Locate every Plasmodium ovale-infected red blood cell.
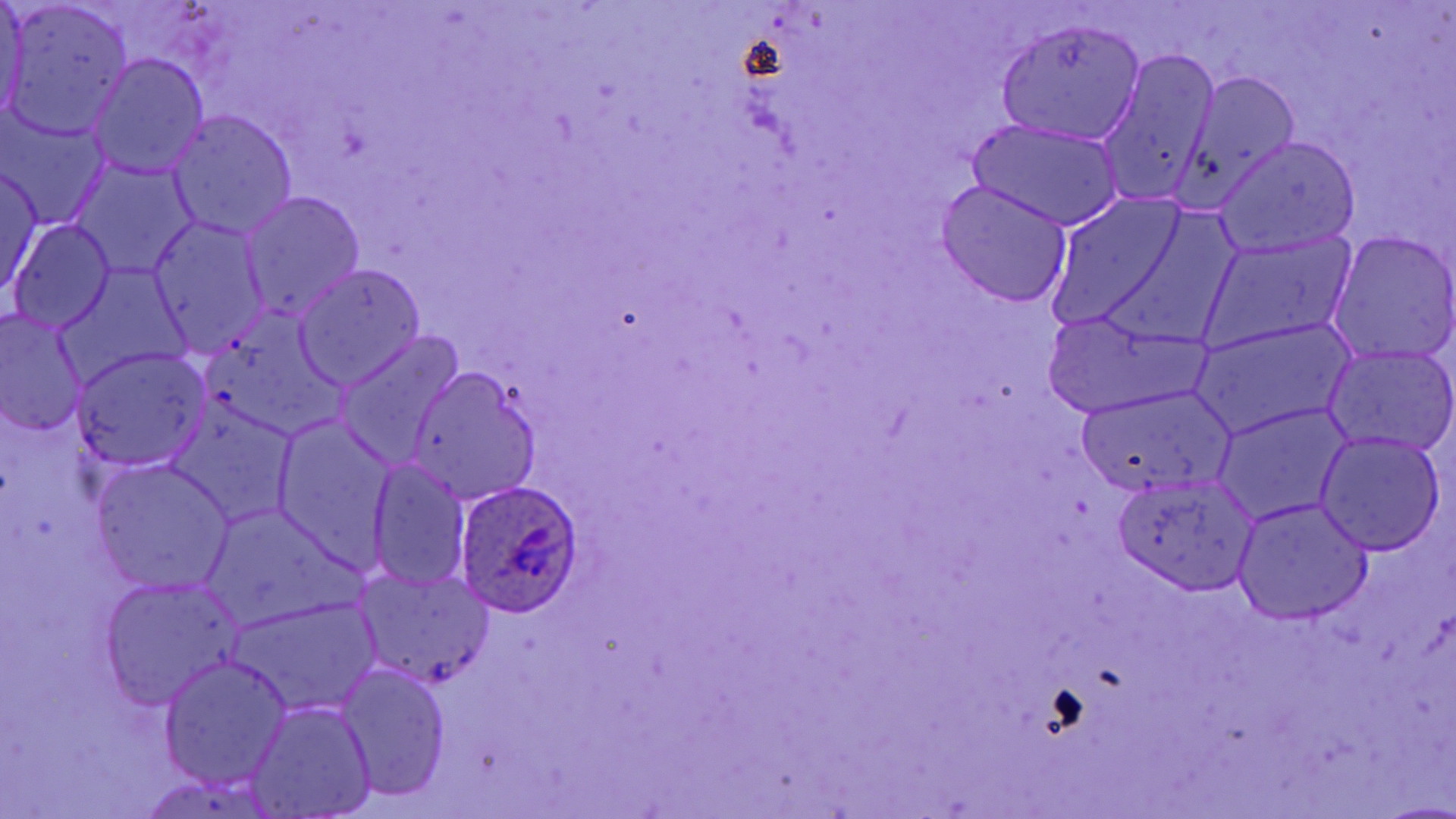
Approximate bounding boxes as [x1, y1, x2, y2] in pixels.
Plasmodium ovale-infected red blood cells: [452, 480, 582, 616].

Uninfected red blood cell locations: [0, 0, 28, 128], [2, 3, 132, 138], [995, 18, 1146, 146], [1096, 49, 1218, 207], [89, 56, 208, 177], [1180, 70, 1299, 199], [168, 110, 297, 240], [2, 113, 108, 229], [966, 120, 1126, 234], [1218, 138, 1361, 259], [75, 163, 193, 276], [1, 166, 45, 298], [937, 182, 1073, 308], [240, 192, 364, 323], [146, 218, 267, 354], [11, 220, 117, 335], [1329, 233, 1456, 364], [1208, 235, 1353, 346], [294, 265, 425, 389], [1037, 311, 1204, 416], [0, 312, 87, 436], [199, 322, 352, 441], [1196, 322, 1354, 437], [337, 332, 461, 468], [1326, 344, 1456, 456], [72, 348, 209, 471], [409, 369, 540, 503], [1077, 387, 1230, 496], [1216, 404, 1352, 523], [270, 415, 399, 567], [1314, 433, 1445, 555], [369, 458, 471, 591], [91, 462, 233, 596], [1114, 475, 1257, 595], [1232, 499, 1373, 625], [205, 508, 348, 627], [358, 572, 494, 691], [100, 579, 238, 708], [233, 599, 377, 715], [160, 655, 292, 787], [336, 663, 452, 801], [248, 702, 377, 818]. Slide-level diagnosis: Plasmodium ovale. Captured at 1000x magnification. Light microscopy. Single field of view. Image is 1456×819 pixels. Thin blood smear. May-Grünwald-Giemsa stain.